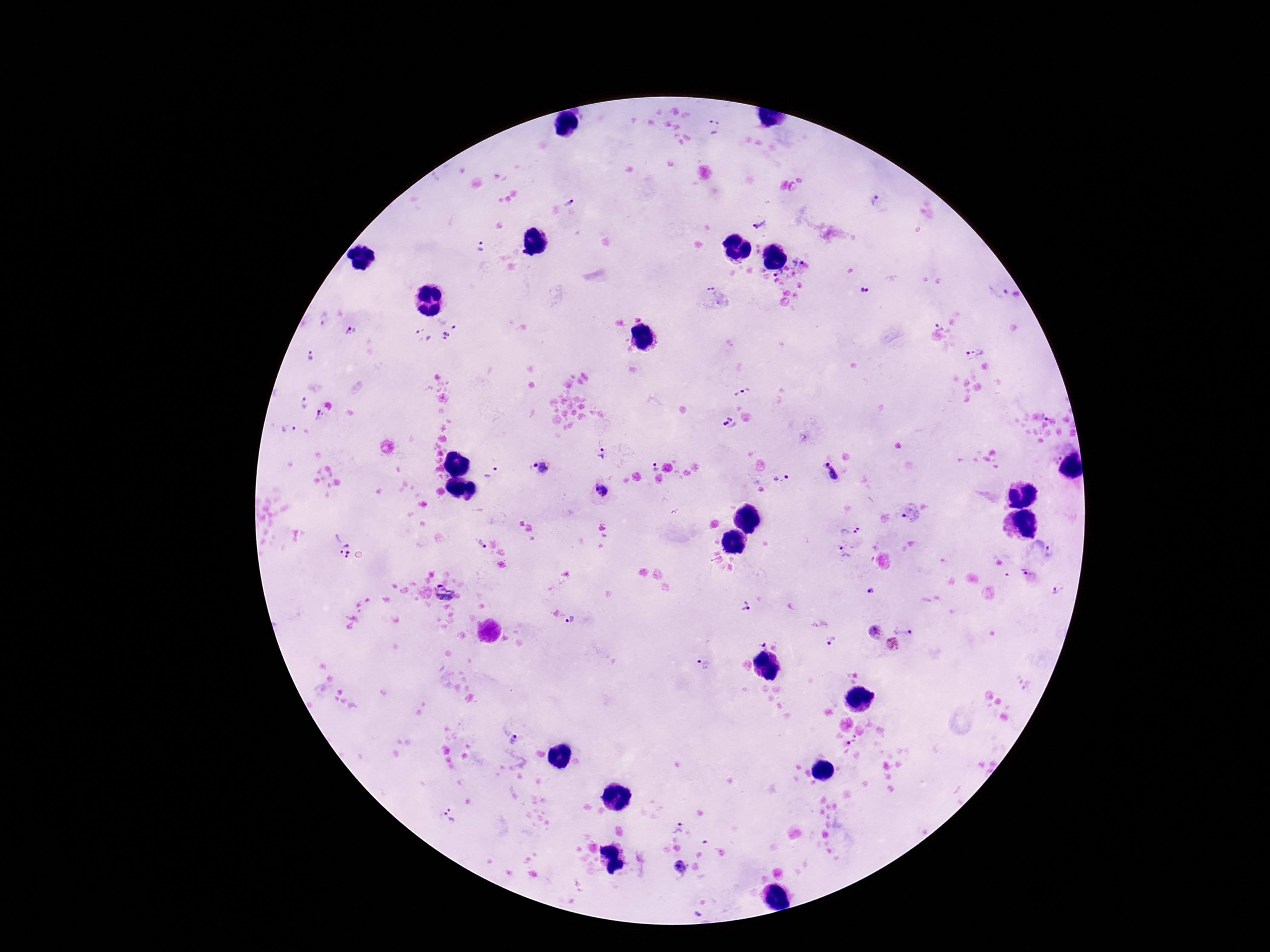

Approximate centers as (x, y) in pixels.
Summary:
  - Plasmodium parasite locations: (714, 127), (875, 201), (570, 202), (759, 224), (480, 245), (778, 274), (864, 289), (712, 292), (999, 292), (323, 319), (939, 326), (351, 331), (438, 339), (975, 353), (311, 355), (743, 389), (304, 404), (319, 416), (1047, 416), (730, 423), (289, 428), (602, 454), (534, 465), (655, 466), (545, 468), (492, 472), (832, 472), (787, 477), (775, 480), (600, 490), (849, 529), (340, 545), (845, 550), (1050, 551), (1027, 572), (1057, 588), (871, 589), (443, 593), (745, 607), (571, 619), (903, 631), (875, 632), (832, 641), (761, 643), (892, 644), (704, 663), (513, 739), (855, 739), (449, 814), (677, 827), (680, 866), (698, 915)
  - Stain: Giemsa
  - Preparation: thick blood film
  - Field of view: single
  - Image size: 1270×952 pixels
  - Capture: smartphone camera through the microscope eyepiece
  - Patient malaria status: positive
  - Magnification: 100x